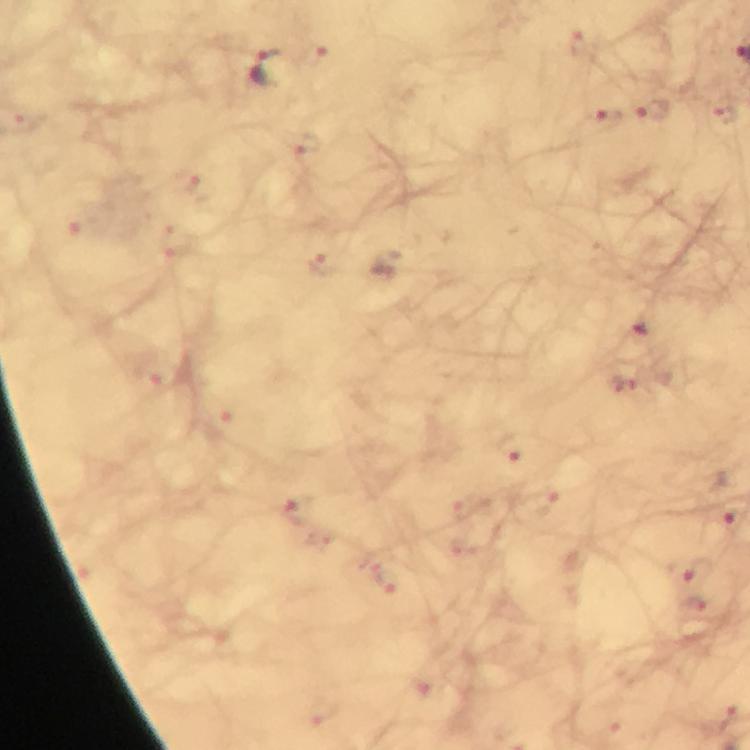
cropped from = a single field of view
magnification = 100x
immersion oil = used
malaria parasite locations = approximate centers as {x, y} in pixels: {580, 45}, {317, 54}, {265, 68}, {653, 111}, {725, 114}, {28, 119}, {607, 119}, {307, 146}, {187, 182}, {79, 223}, {176, 240}, {322, 263}, {640, 329}, {157, 370}, {621, 384}, {218, 419}, {512, 444}, {545, 499}, {465, 507}, {296, 508}, {733, 517}, {320, 537}, {463, 547}, {690, 572}, {381, 577}, {699, 606}, {419, 688}, {319, 715}, {728, 718}
image size = 750×750 pixels
stain = Giemsa
context = from a malaria diagnostic workup
capture = smartphone photograph through a microscope
preparation = thick blood film